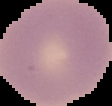

Summary:
  - Image size: 112×106 pixels
  - Preparation: thin blood film
  - Image type: segmented cell region on a black background
  - Malaria status: uninfected